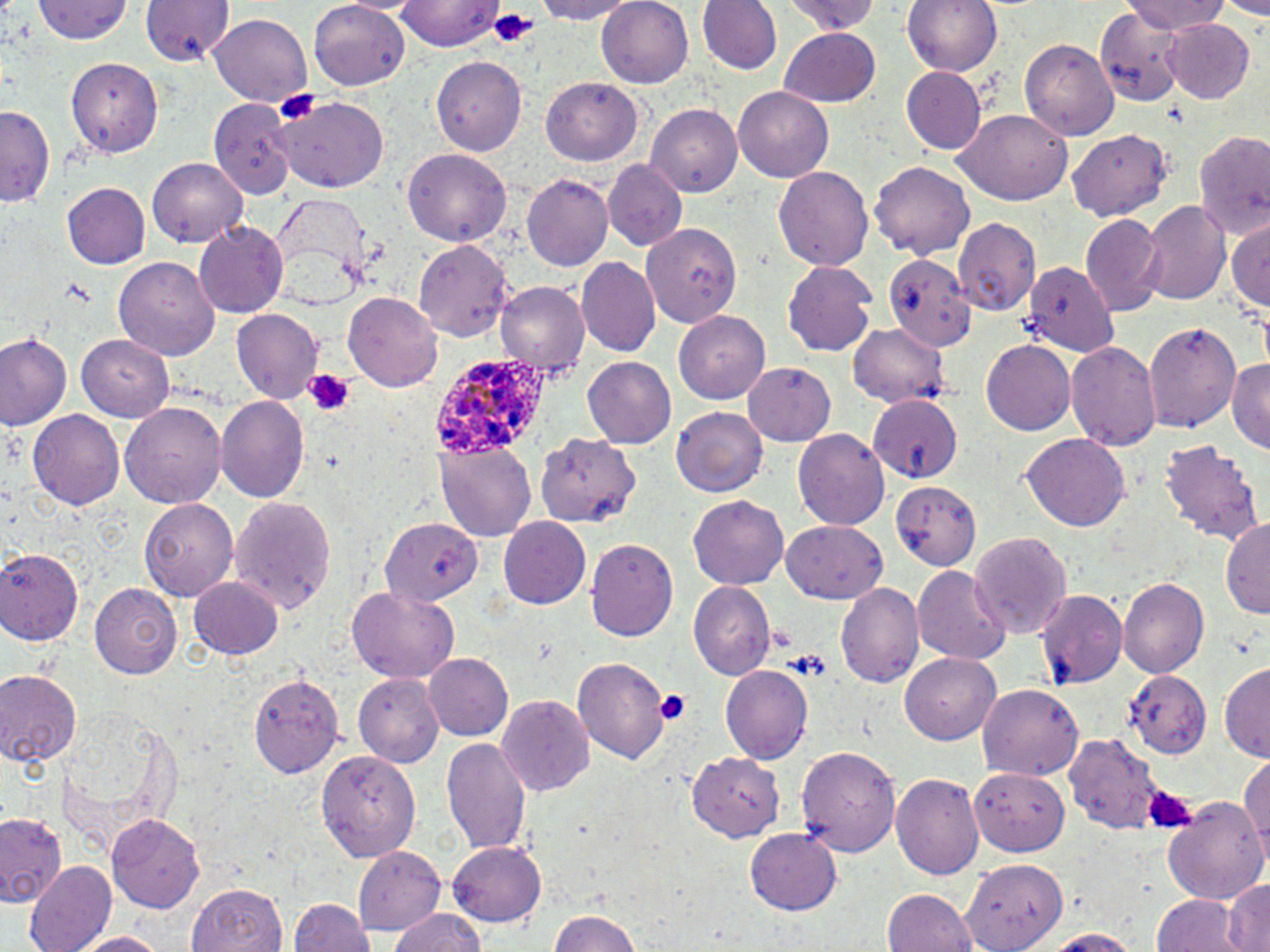

Approximate bounding boxes as (x1, y1, x2, y2) in pixels. Plasmodium ovale-infected red blood cell locations: (433, 357, 557, 456). Platelet locations: (488, 10, 538, 50), (273, 88, 320, 127), (302, 369, 355, 416), (653, 687, 692, 725), (1140, 786, 1196, 834). Uninfected red blood cell locations: (36, 0, 133, 46), (140, 0, 232, 67), (398, 0, 503, 51), (527, 0, 640, 24), (596, 0, 693, 89), (696, 0, 781, 76), (778, 0, 887, 35), (899, 0, 1004, 78), (1216, 0, 1270, 18), (1129, 1, 1231, 37), (309, 3, 408, 88), (1094, 7, 1183, 105), (209, 14, 311, 107), (1165, 19, 1255, 103), (778, 27, 883, 108), (1022, 38, 1119, 142), (432, 55, 527, 155), (68, 58, 164, 157), (900, 67, 985, 153), (541, 77, 644, 165), (735, 86, 835, 181), (212, 96, 296, 198), (274, 98, 389, 191), (643, 104, 741, 197), (0, 105, 53, 211), (954, 109, 1074, 207), (1193, 128, 1270, 241), (1067, 130, 1170, 221), (403, 147, 511, 248), (149, 158, 246, 248), (603, 160, 688, 250), (870, 161, 976, 262), (772, 165, 876, 274), (520, 172, 612, 270), (57, 173, 227, 263), (63, 183, 148, 270), (269, 195, 373, 303), (1140, 199, 1230, 307), (1081, 213, 1164, 316), (954, 218, 1041, 314), (1228, 219, 1270, 312), (645, 222, 741, 326), (195, 224, 286, 316), (414, 240, 515, 342), (882, 249, 972, 364), (112, 255, 220, 359), (577, 258, 660, 356), (782, 259, 877, 357), (1023, 265, 1117, 356), (497, 282, 588, 378), (344, 291, 443, 391), (231, 310, 322, 404), (675, 312, 771, 403), (1144, 319, 1240, 432), (848, 322, 947, 406), (2, 332, 71, 432), (75, 333, 174, 421), (981, 338, 1076, 436), (1067, 341, 1160, 451), (1229, 356, 1270, 451), (581, 358, 675, 449), (742, 362, 835, 445), (867, 394, 962, 485), (215, 396, 310, 504), (122, 403, 228, 508), (671, 407, 767, 496), (27, 410, 124, 511), (794, 429, 891, 531), (533, 430, 638, 526), (1020, 432, 1132, 531), (436, 438, 537, 540), (1158, 439, 1266, 549), (894, 484, 977, 572), (688, 493, 789, 589), (227, 495, 337, 614), (139, 498, 237, 599), (498, 516, 590, 610), (382, 518, 482, 606), (782, 519, 889, 604), (1222, 520, 1270, 620), (794, 527, 917, 649), (971, 531, 1071, 642), (586, 538, 679, 643), (1, 544, 83, 645), (914, 566, 1009, 666), (188, 576, 282, 659), (1120, 578, 1208, 679), (689, 581, 775, 680), (836, 581, 924, 689), (90, 584, 180, 679), (347, 587, 459, 682), (1038, 589, 1127, 690), (423, 652, 513, 740), (899, 652, 1002, 745), (574, 655, 670, 767), (720, 662, 812, 759), (1219, 662, 1270, 759), (0, 668, 83, 767), (1123, 669, 1210, 757), (250, 671, 345, 779), (356, 672, 447, 767), (978, 685, 1085, 780), (498, 694, 595, 797), (57, 708, 176, 837), (1060, 728, 1179, 836), (442, 736, 530, 856), (797, 745, 901, 857), (318, 748, 421, 861), (686, 749, 784, 842), (1238, 758, 1270, 860), (969, 769, 1067, 856), (891, 773, 983, 880), (1165, 795, 1269, 907), (2, 809, 64, 906), (107, 812, 208, 913), (745, 828, 843, 913), (449, 841, 548, 926), (355, 846, 446, 931), (959, 847, 1071, 950), (23, 860, 115, 952), (1222, 876, 1269, 952), (359, 880, 467, 952), (186, 881, 290, 952), (881, 889, 976, 952), (1150, 894, 1242, 952), (288, 898, 376, 951), (386, 910, 488, 952), (542, 910, 645, 952), (1038, 927, 1145, 951), (68, 930, 174, 951). Slide-level diagnosis: Plasmodium ovale. Optical microscopy. Thin blood film. May-Grünwald-Giemsa-stained preparation. Single field of view. Captured at 1000x magnification. Image is 1270×952 pixels.